Classify this cell by malaria status.
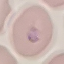
Parasitized.

preparation: thin blood smear
stain: Giemsa
capture: smartphone through the microscope eyepiece
image_type: cell patch, automatically extracted from a larger field of view and resized to 64 × 64 pixels